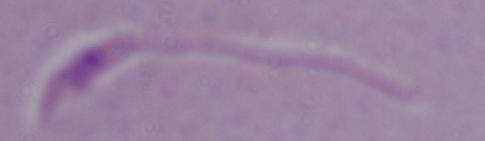
Summary:
  - Magnification: 1000x
  - Modality: micrograph
  - Identification: Leishmania